Describe the morphology of the red blood cells.
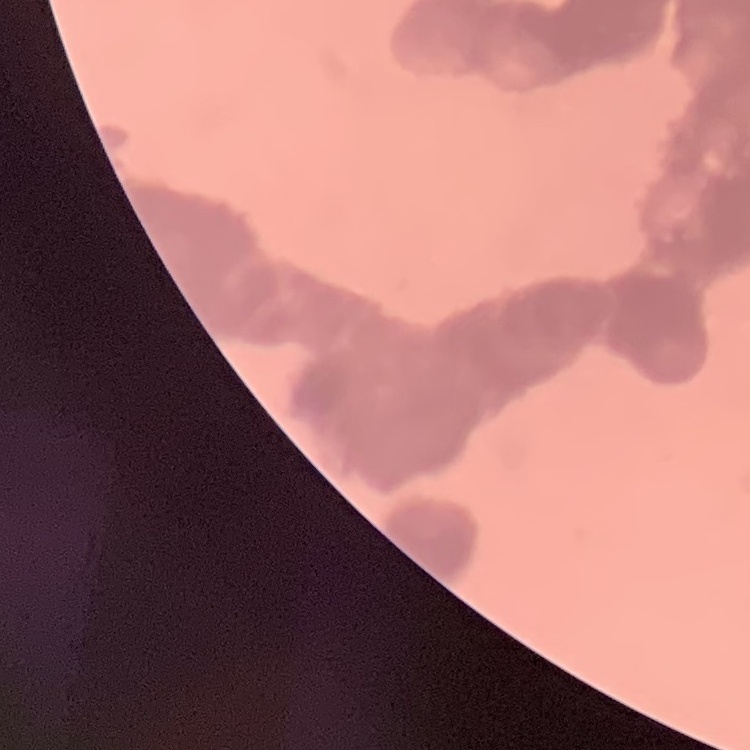
They show rouleaux formation.

Summary:
  - Preparation: thin peripheral smear
  - Stain: Field's or Giemsa
  - Image type: square crop of a larger photomicrograph